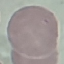

result = negative for malaria parasites
image type = cell patch, automatically extracted from a larger field of view and resized to 64 × 64 pixels
capture = smartphone camera at the microscope eyepiece
preparation = thin blood film
stain = Giemsa